Name the blood parasite species.
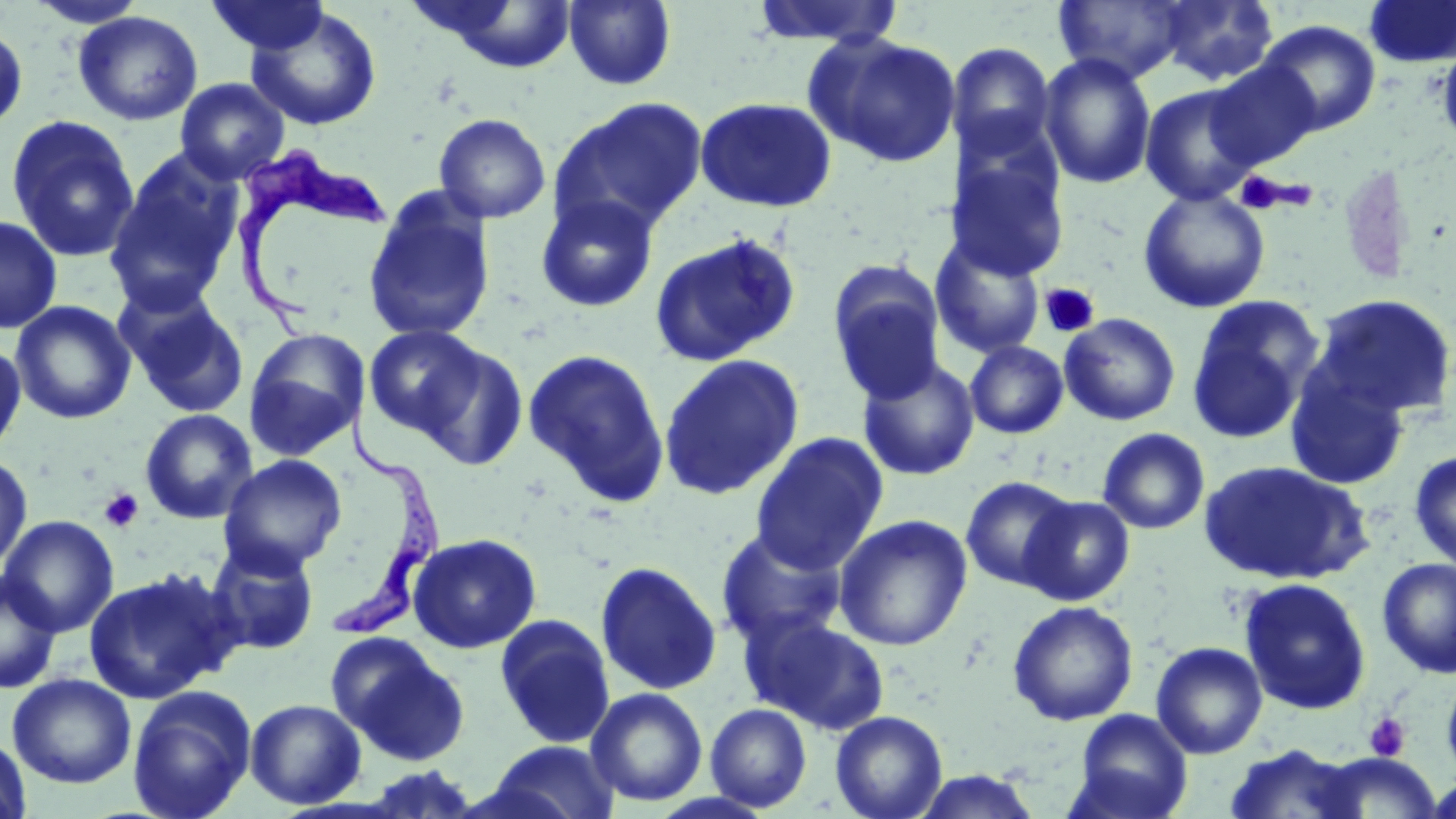
Trypanosoma brucei.

Summary:
  - Coordinate format: approximate bounding boxes as [x1, y1, x2, y2] in pixels
  - Trypanosoma brucei locations: [226, 145, 393, 338], [330, 398, 442, 634]
  - Platelet locations: [1234, 172, 1294, 213], [1039, 282, 1100, 338], [100, 488, 144, 533], [1364, 712, 1411, 762]
  - Uninfected red blood cell locations: [25, 0, 149, 28], [205, 0, 331, 57], [564, 0, 676, 90], [1053, 0, 1191, 84], [1157, 0, 1279, 86], [1363, 0, 1456, 68], [748, 1, 907, 48], [412, 2, 581, 72], [245, 7, 383, 132], [73, 11, 203, 126], [1256, 20, 1381, 136], [0, 21, 28, 134], [804, 32, 962, 168], [1436, 38, 1456, 153], [947, 42, 1056, 159], [1038, 52, 1156, 189], [1205, 61, 1321, 169], [175, 78, 290, 185], [1140, 83, 1263, 205], [694, 96, 838, 212], [550, 97, 708, 237], [433, 112, 552, 224], [5, 114, 141, 263], [105, 151, 245, 314], [947, 153, 1069, 281], [1137, 189, 1270, 313], [362, 190, 496, 344], [535, 193, 660, 313], [0, 215, 62, 334], [649, 232, 802, 369], [930, 235, 1046, 359], [827, 263, 947, 403], [118, 288, 250, 419], [1306, 293, 1456, 422], [1187, 297, 1324, 444], [10, 300, 136, 425], [1059, 313, 1181, 426], [364, 324, 488, 440], [243, 328, 369, 460], [0, 338, 26, 461], [965, 340, 1069, 439], [414, 342, 528, 469], [523, 348, 671, 505], [658, 354, 805, 499], [857, 357, 980, 481], [1284, 368, 1411, 491], [139, 408, 259, 525], [1098, 428, 1210, 534], [750, 432, 888, 574], [1409, 449, 1456, 573], [0, 451, 33, 575], [218, 454, 348, 576], [1198, 460, 1371, 586], [960, 475, 1078, 591], [1021, 495, 1134, 606], [834, 514, 973, 651], [0, 515, 119, 637], [715, 527, 850, 649], [407, 533, 542, 654], [205, 540, 320, 656], [1377, 557, 1456, 678], [595, 560, 723, 696], [84, 567, 239, 704], [0, 570, 63, 694], [1237, 577, 1372, 715], [1007, 601, 1139, 726], [494, 614, 616, 749], [744, 614, 891, 735], [327, 633, 471, 767], [1151, 641, 1267, 759], [1441, 666, 1456, 789], [7, 673, 136, 789], [127, 685, 257, 819], [586, 687, 708, 807], [245, 698, 366, 809], [705, 703, 813, 812], [1068, 709, 1193, 819], [830, 710, 947, 819], [0, 732, 33, 819], [481, 740, 621, 819], [1222, 743, 1367, 819], [1313, 755, 1441, 817], [354, 765, 486, 819], [910, 769, 1044, 818]
  - Magnification: 1000x
  - Image size: 1456×819 pixels
  - Modality: optical microscopy
  - Preparation: thin blood film
  - Stain: May-Grünwald-Giemsa
  - Field of view: single